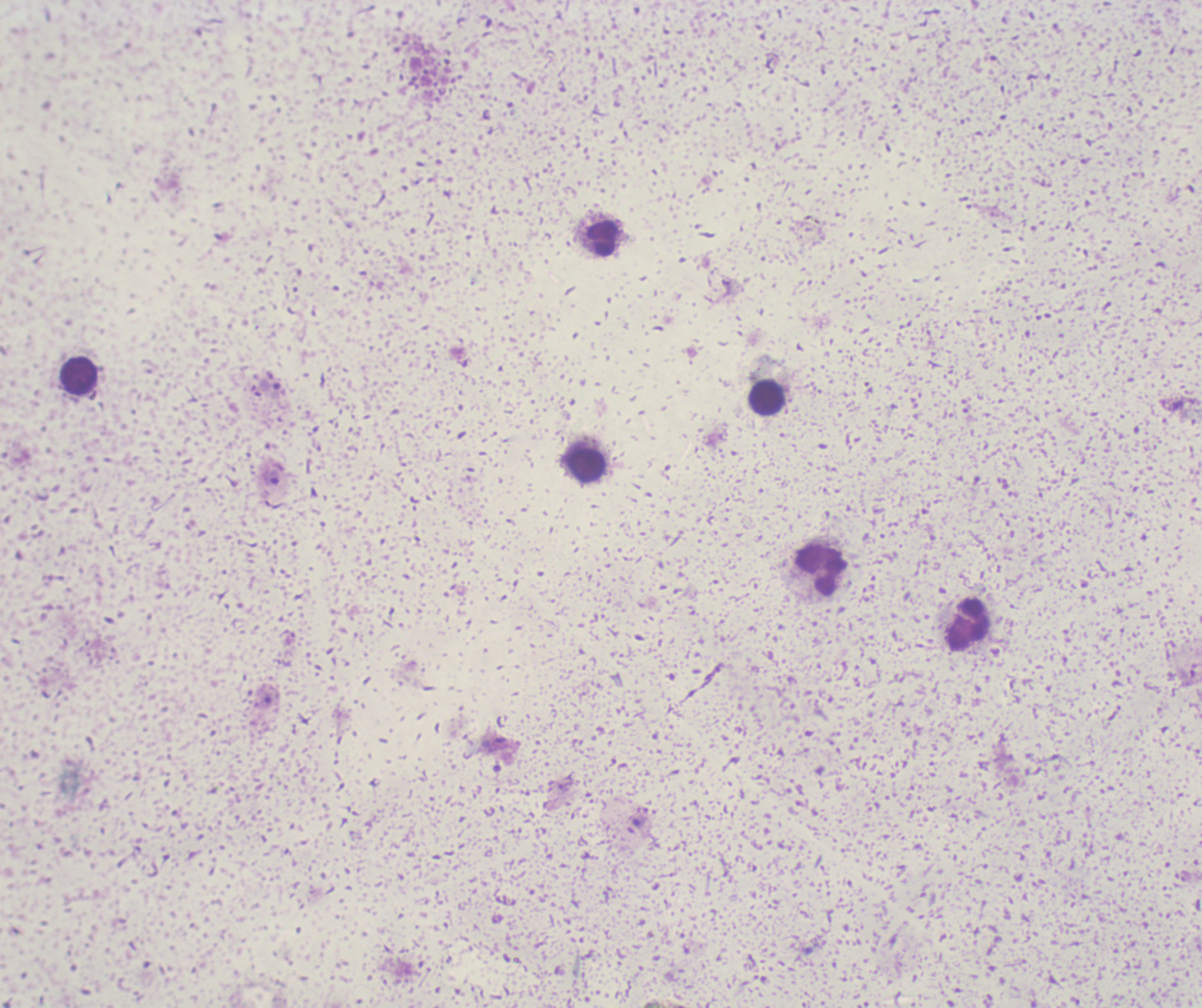

Approximate centers as (x, y) in pixels.
Summary:
  - Leukocyte locations: (601, 238), (79, 376), (768, 397), (586, 465), (821, 570), (968, 626)
  - Trophozoite locations: (274, 477), (640, 822)
  - Background quality: unsatisfactory
  - Stain: Romanowsky
  - Image size: 1202×1008 pixels
  - Field of view: single
  - Preparation: thick blood smear
  - Magnification: 100x
  - Result: malaria parasites detected
  - Context: previously used in an actual diagnosis